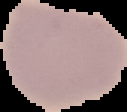

malaria_status: uninfected
image_size: 127×112 pixels
preparation: thin blood film
image_type: segmented cell region with the area outside set to black